Comment on the morphology of the red blood cells.
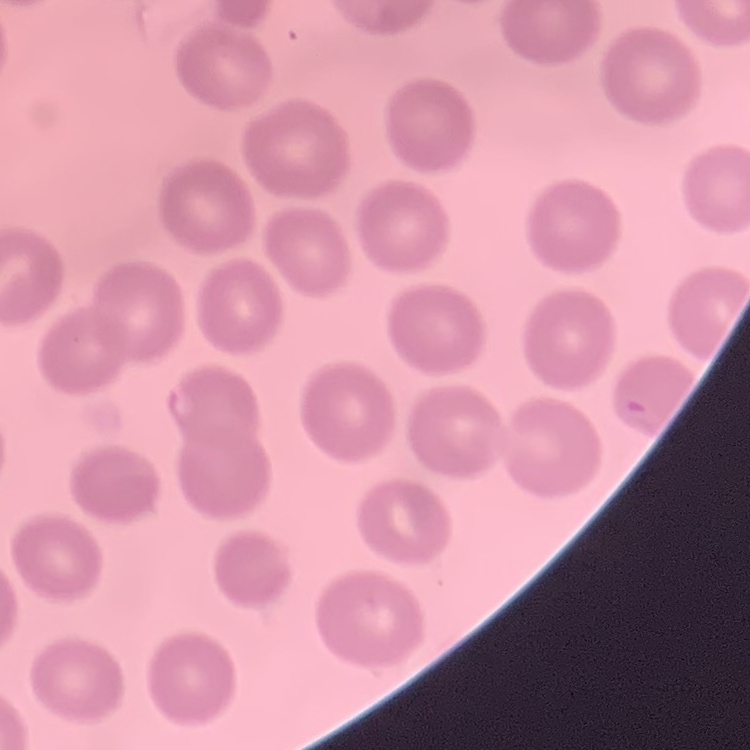
They show no rouleaux formation.

Summary:
  - Stain: Field's or Giemsa
  - Preparation: thin peripheral smear
  - Image type: square crop of a larger photomicrograph